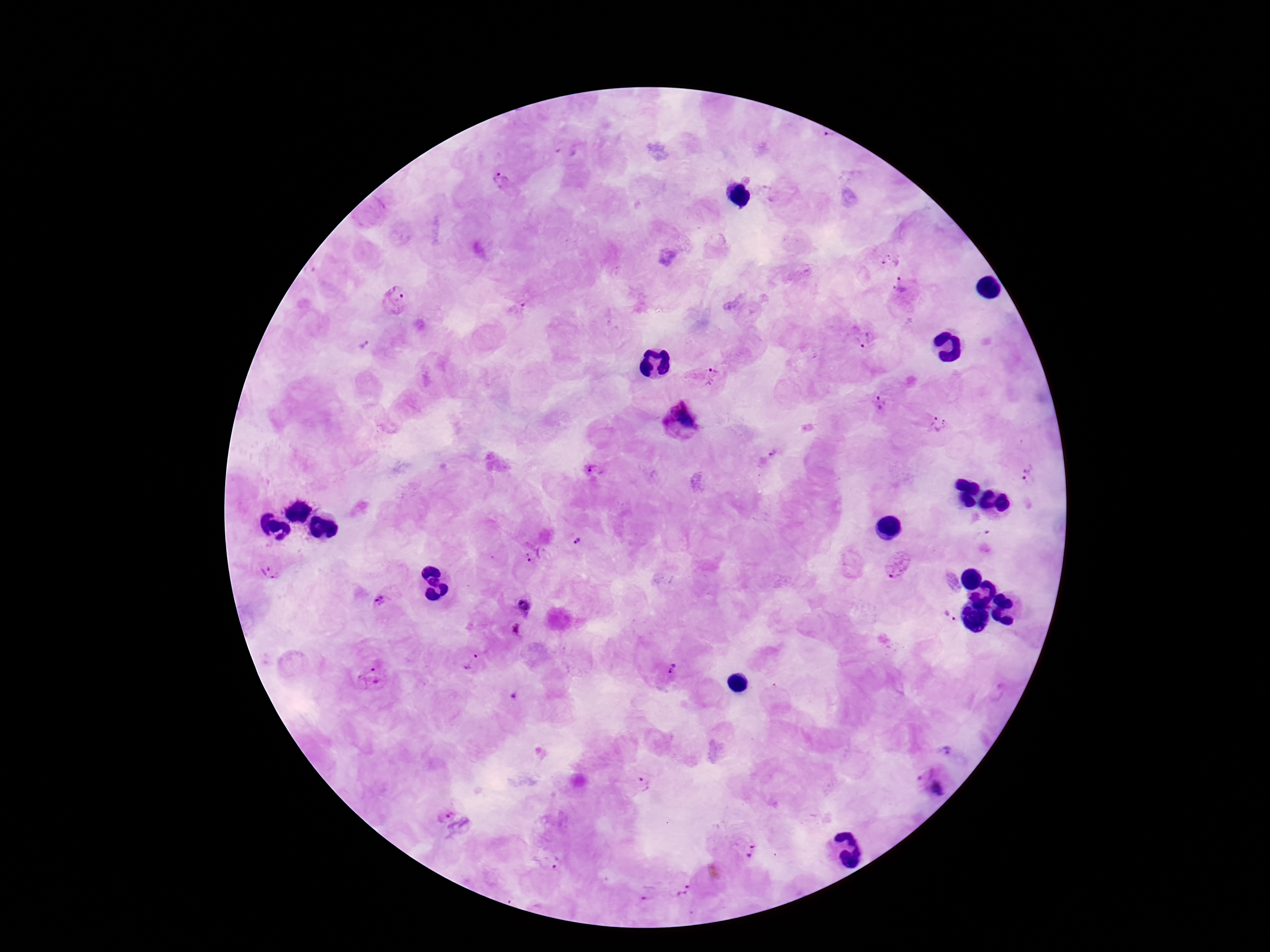

{
  "image_size": "1270×952 pixels",
  "preparation": "thick blood smear",
  "magnification": "100x",
  "patient_malaria_status": "positive",
  "field_of_view": "single",
  "stain": "Giemsa",
  "plasmodium_parasite_locations": "approximate centers as (x, y) in pixels: (501, 180), (889, 257), (905, 293), (398, 302), (520, 309), (864, 339), (363, 344), (707, 377), (882, 404), (683, 420), (940, 424), (772, 453), (594, 470), (1029, 477), (985, 537), (578, 541), (537, 555), (896, 565), (271, 569), (382, 599), (527, 605), (949, 616), (516, 631), (473, 661), (672, 667), (372, 676), (516, 697), (947, 752), (933, 784), (641, 785), (456, 819), (747, 848), (549, 861), (686, 892), (649, 893)",
  "capture": "smartphone camera through the microscope eyepiece"
}